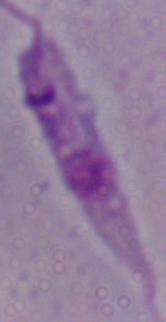
modality: photomicrograph
magnification: 1000x
identification: Leishmania